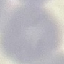

Summary:
  - Malaria status: uninfected
  - Capture: smartphone through the microscope eyepiece
  - Stain: Giemsa
  - Image type: cell patch, automatically extracted from a larger field of view and resized to 64 × 64 pixels
  - Preparation: thin blood film